Look for Plasmodium parasites.
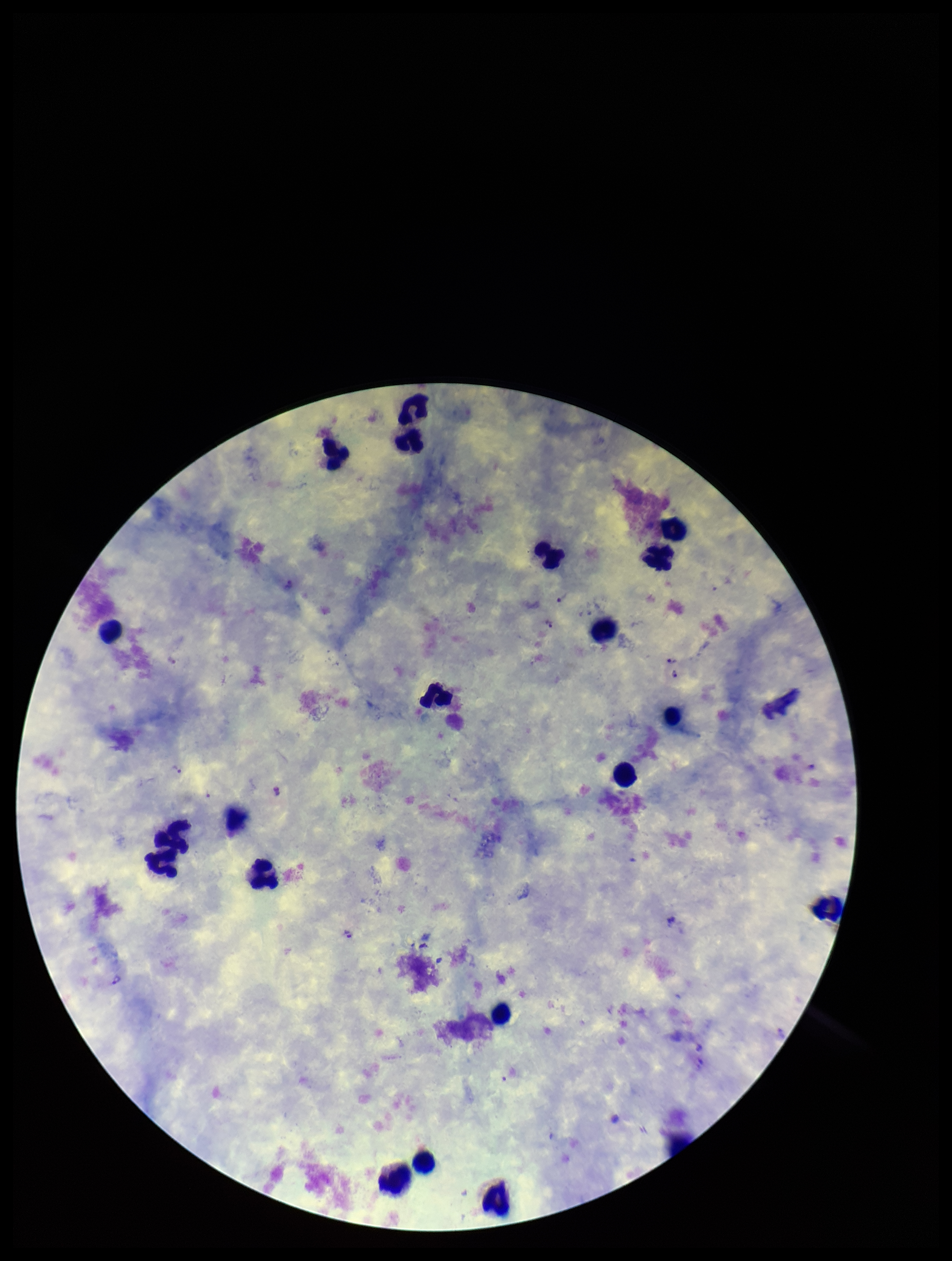

Detected.

Parasite count: 10. Leukocyte count: 19. Single field of view. Patient malaria status: infected. Photographed through the microscope eyepiece with a smartphone camera. Species reported for this patient: Plasmodium vivax. Image is 952×1261 pixels. Giemsa stain. Preparation: thick.